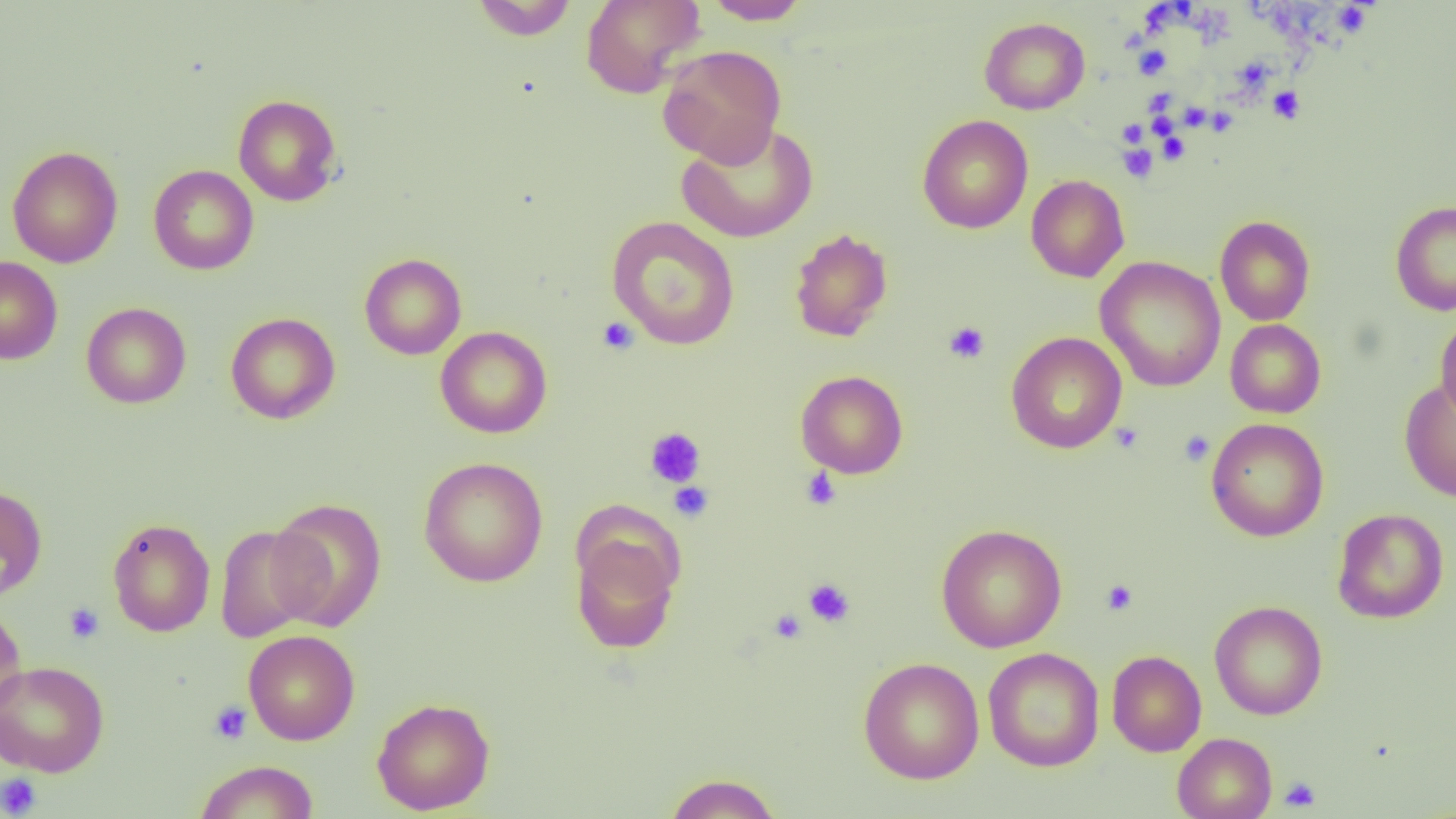
Summary:
  - Coordinate format: approximate bounding boxes as (x1, y1, x2, y2) in pixels
  - Uninfected red blood cell locations: (471, 0, 578, 40), (580, 0, 705, 98), (702, 0, 811, 25), (979, 17, 1090, 115), (657, 44, 786, 166), (233, 94, 343, 207), (917, 114, 1033, 233), (676, 121, 819, 244), (7, 146, 123, 268), (148, 165, 259, 275), (1026, 175, 1129, 283), (1390, 200, 1456, 316), (1214, 215, 1315, 326), (606, 216, 740, 350), (789, 227, 893, 342), (359, 253, 467, 360), (0, 256, 63, 364), (1095, 256, 1226, 392), (81, 302, 191, 408), (225, 312, 341, 425), (1435, 316, 1456, 423), (1225, 319, 1325, 418), (435, 326, 552, 438), (1005, 331, 1127, 453), (795, 370, 908, 478), (1399, 379, 1456, 502), (1206, 418, 1329, 541), (418, 457, 548, 587), (0, 484, 48, 601), (267, 497, 388, 632), (1332, 508, 1449, 623), (107, 517, 215, 637), (935, 523, 1067, 653), (213, 524, 323, 643), (570, 530, 682, 655), (1210, 600, 1328, 720), (0, 602, 28, 721), (243, 629, 360, 745), (983, 647, 1105, 772), (1107, 650, 1207, 756), (858, 657, 984, 784), (0, 660, 110, 777), (371, 696, 495, 815), (1172, 732, 1277, 819), (193, 759, 320, 818), (663, 772, 782, 818)
  - Platelet locations: (1332, 3, 1373, 37), (1144, 9, 1176, 35), (1134, 46, 1171, 79), (1233, 60, 1270, 84), (1268, 86, 1305, 123), (1146, 90, 1177, 111), (1184, 108, 1208, 132), (1212, 110, 1236, 139), (1148, 115, 1182, 137), (1118, 119, 1148, 147), (1157, 132, 1189, 164), (1118, 143, 1158, 182), (597, 316, 639, 355), (944, 321, 990, 364), (1110, 421, 1145, 454), (644, 427, 706, 488), (1178, 430, 1213, 466), (800, 468, 842, 511), (668, 482, 714, 523), (803, 578, 855, 627), (1100, 579, 1138, 615), (64, 602, 105, 644), (768, 608, 807, 644), (208, 701, 252, 744), (0, 772, 42, 818), (1278, 776, 1321, 812)
  - Slide-level diagnosis: negative for blood parasites
  - Field of view: one of a larger specimen
  - Magnification: 1000x
  - Image size: 1456×819 pixels
  - Modality: optical microscopy
  - Preparation: thin blood film